Locate every Plasmodium parasite.
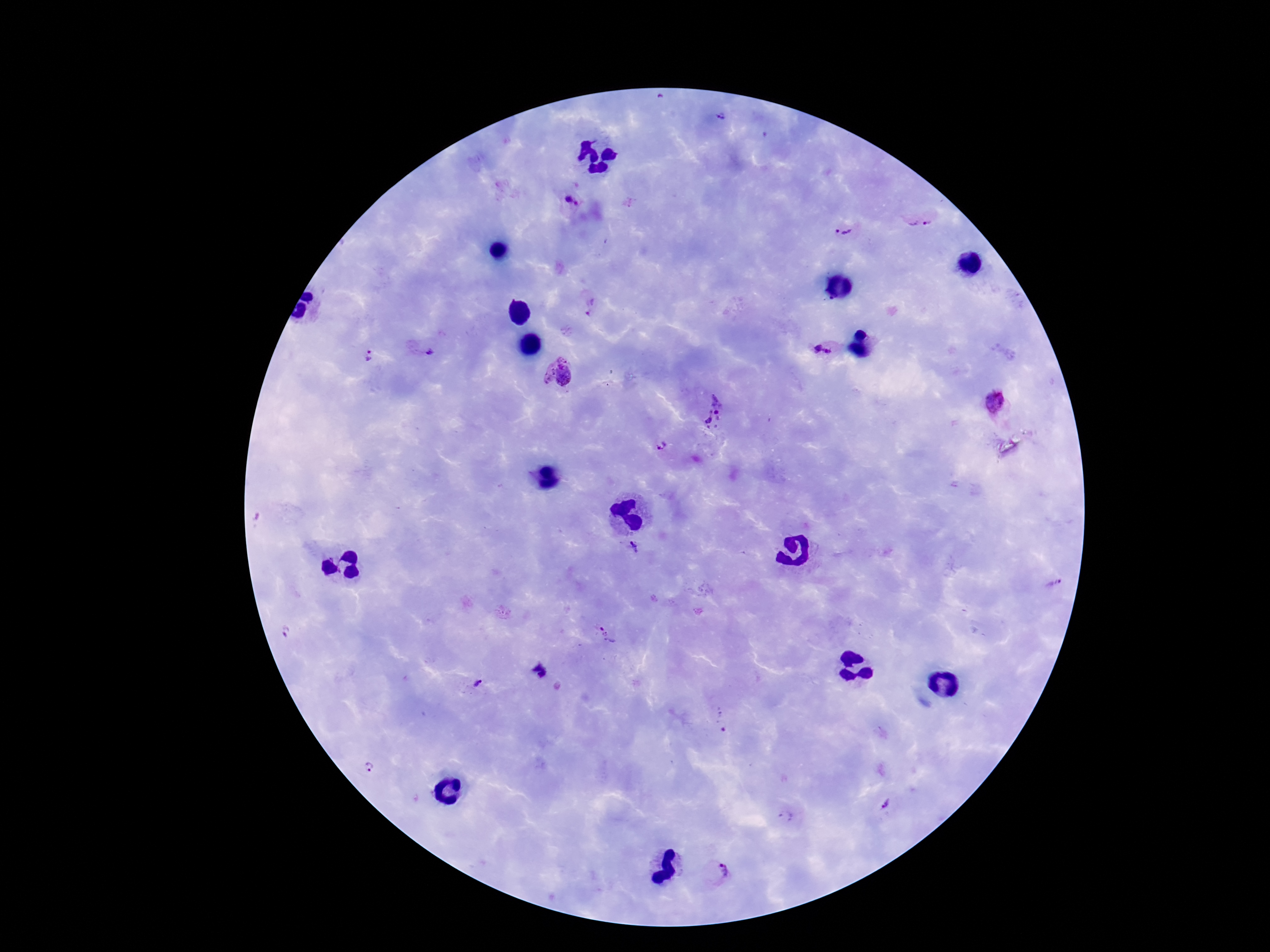
Approximate object centers, in pixels from the top-left corner.
Plasmodium parasites: (x=721, y=116), (x=570, y=203), (x=919, y=221), (x=844, y=229), (x=592, y=308), (x=821, y=346), (x=424, y=350), (x=370, y=358), (x=558, y=376), (x=994, y=402), (x=717, y=412), (x=660, y=448), (x=634, y=548), (x=600, y=628), (x=286, y=632), (x=540, y=670), (x=478, y=685), (x=720, y=720), (x=368, y=767), (x=887, y=806), (x=786, y=819), (x=719, y=873).

patient malaria status = positive
magnification = 100x
image size = 1270×952 pixels
capture = smartphone camera through the microscope eyepiece
preparation = thick peripheral-blood smear
field of view = single
stain = Giemsa